Report the malaria status of this cell.
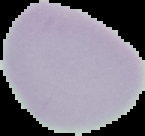

Uninfected.

Image is 145×136 pixels. The area outside the segmented cell region is set to black. From a thin blood smear.